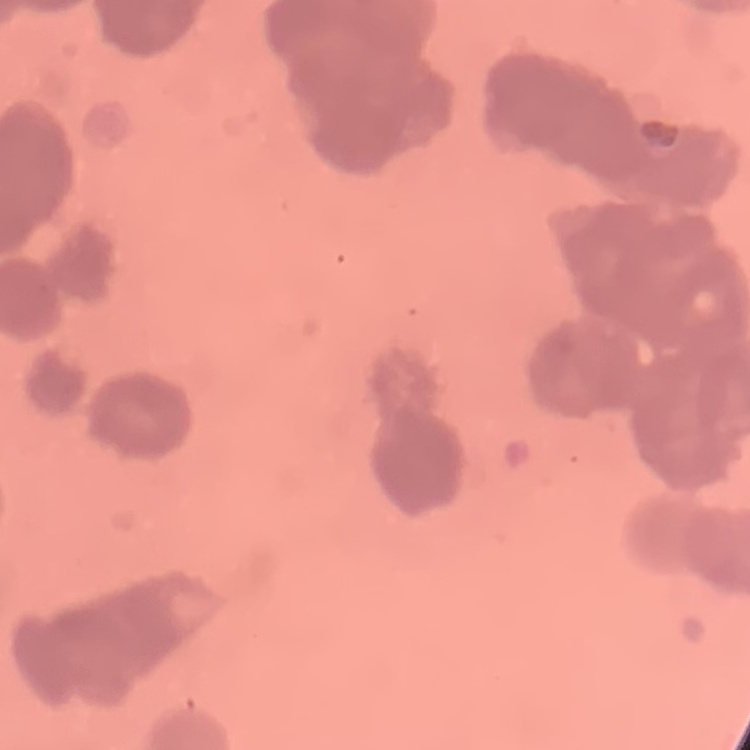

red blood cell morphology = rouleaux formation
stain = Field's or Giemsa
preparation = thin blood smear
image type = one tile cut from a larger photomicrograph